Give the extent of all uninfected red blood cells.
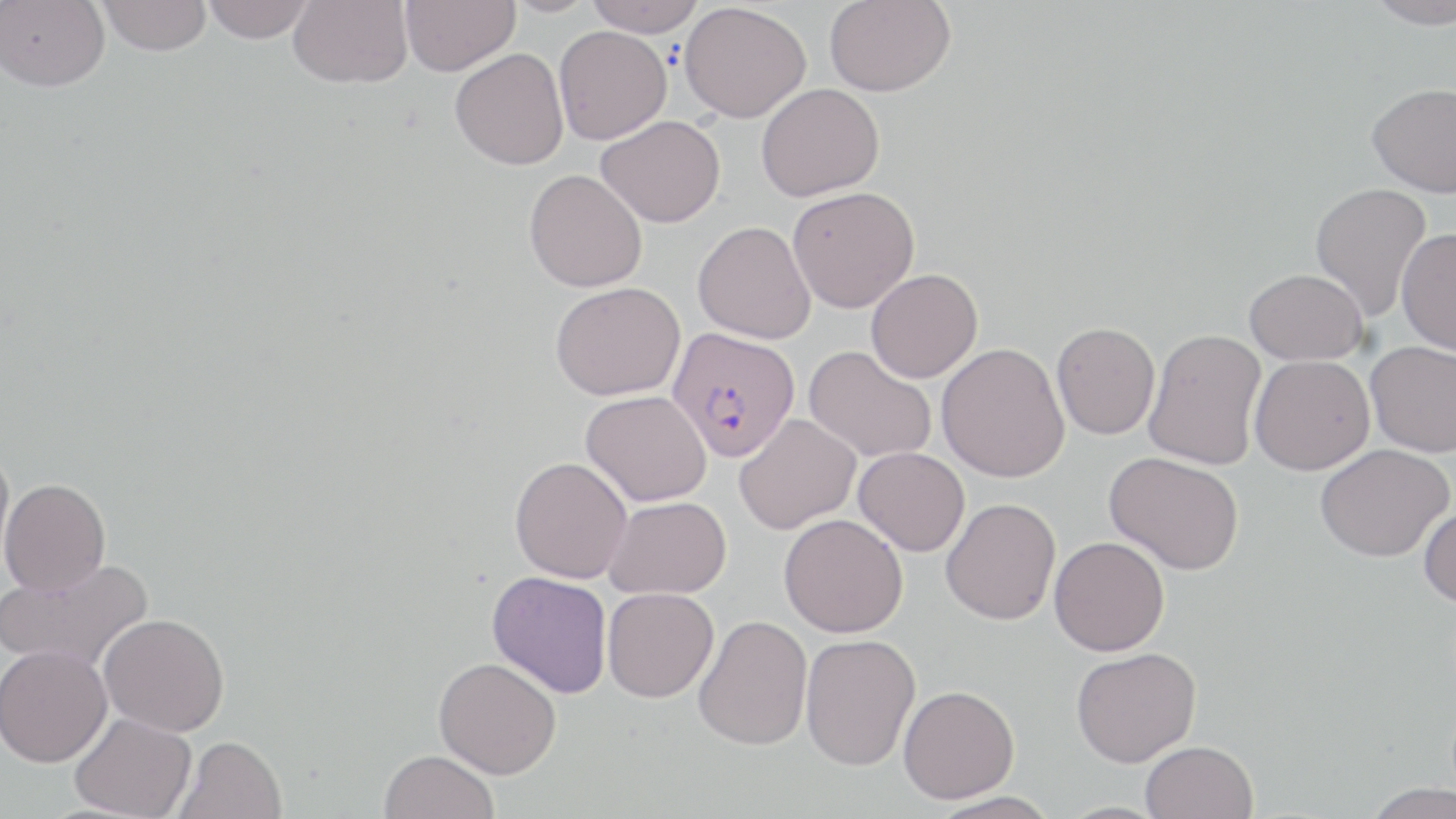
Approximate bounding boxes as named x1/y1/x2/y2 corners in pixels.
Uninfected red blood cells: (x1=0, y1=0, x2=109, y2=92), (x1=97, y1=0, x2=212, y2=56), (x1=202, y1=0, x2=314, y2=42), (x1=288, y1=0, x2=413, y2=88), (x1=400, y1=0, x2=519, y2=76), (x1=502, y1=0, x2=598, y2=17), (x1=585, y1=0, x2=705, y2=36), (x1=824, y1=0, x2=956, y2=96), (x1=1364, y1=0, x2=1455, y2=29), (x1=679, y1=2, x2=811, y2=123), (x1=554, y1=26, x2=671, y2=144), (x1=450, y1=48, x2=569, y2=170), (x1=756, y1=83, x2=884, y2=201), (x1=1367, y1=83, x2=1456, y2=196), (x1=596, y1=115, x2=725, y2=227), (x1=524, y1=169, x2=648, y2=293), (x1=1310, y1=182, x2=1432, y2=322), (x1=787, y1=186, x2=919, y2=313), (x1=692, y1=221, x2=816, y2=344), (x1=1396, y1=229, x2=1456, y2=356), (x1=1244, y1=268, x2=1367, y2=365), (x1=865, y1=269, x2=982, y2=382), (x1=550, y1=281, x2=685, y2=401), (x1=1051, y1=322, x2=1160, y2=439), (x1=1144, y1=328, x2=1267, y2=471), (x1=1365, y1=340, x2=1456, y2=458), (x1=937, y1=343, x2=1070, y2=482), (x1=804, y1=346, x2=936, y2=463), (x1=1249, y1=355, x2=1374, y2=474), (x1=582, y1=390, x2=712, y2=506), (x1=735, y1=414, x2=860, y2=534), (x1=0, y1=444, x2=15, y2=575), (x1=1315, y1=444, x2=1453, y2=561), (x1=854, y1=447, x2=969, y2=556), (x1=1104, y1=452, x2=1244, y2=575), (x1=510, y1=456, x2=632, y2=583), (x1=1, y1=478, x2=110, y2=595), (x1=603, y1=496, x2=732, y2=599), (x1=940, y1=497, x2=1061, y2=625), (x1=1418, y1=504, x2=1456, y2=607), (x1=779, y1=513, x2=908, y2=638), (x1=1049, y1=536, x2=1170, y2=656), (x1=0, y1=558, x2=152, y2=675), (x1=487, y1=571, x2=613, y2=698), (x1=602, y1=587, x2=718, y2=702), (x1=99, y1=613, x2=230, y2=736), (x1=693, y1=615, x2=813, y2=750), (x1=800, y1=633, x2=921, y2=771), (x1=0, y1=645, x2=112, y2=766), (x1=1070, y1=647, x2=1201, y2=767), (x1=434, y1=657, x2=562, y2=778), (x1=898, y1=684, x2=1019, y2=803), (x1=69, y1=712, x2=197, y2=819), (x1=174, y1=735, x2=288, y2=819), (x1=1141, y1=740, x2=1259, y2=819), (x1=379, y1=750, x2=499, y2=819), (x1=1360, y1=782, x2=1456, y2=819), (x1=926, y1=790, x2=1063, y2=817).

Summary:
  - Plasmodium falciparum-infected red blood cell locations: (x1=667, y1=326, x2=800, y2=462)
  - Slide-level diagnosis: Plasmodium falciparum
  - Magnification: 1000x
  - Modality: optical microscopy
  - Field of view: single
  - Image size: 1456×819 pixels
  - Preparation: thin blood smear
  - Stain: May-Grünwald-Giemsa